Classify this cell by malaria status.
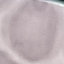
It is uninfected.

Cell patch, automatically extracted from a larger field of view and resized to 64 × 64 pixels. Acquired by smartphone through the microscope eyepiece. Thin smear of blood. Giemsa stain.